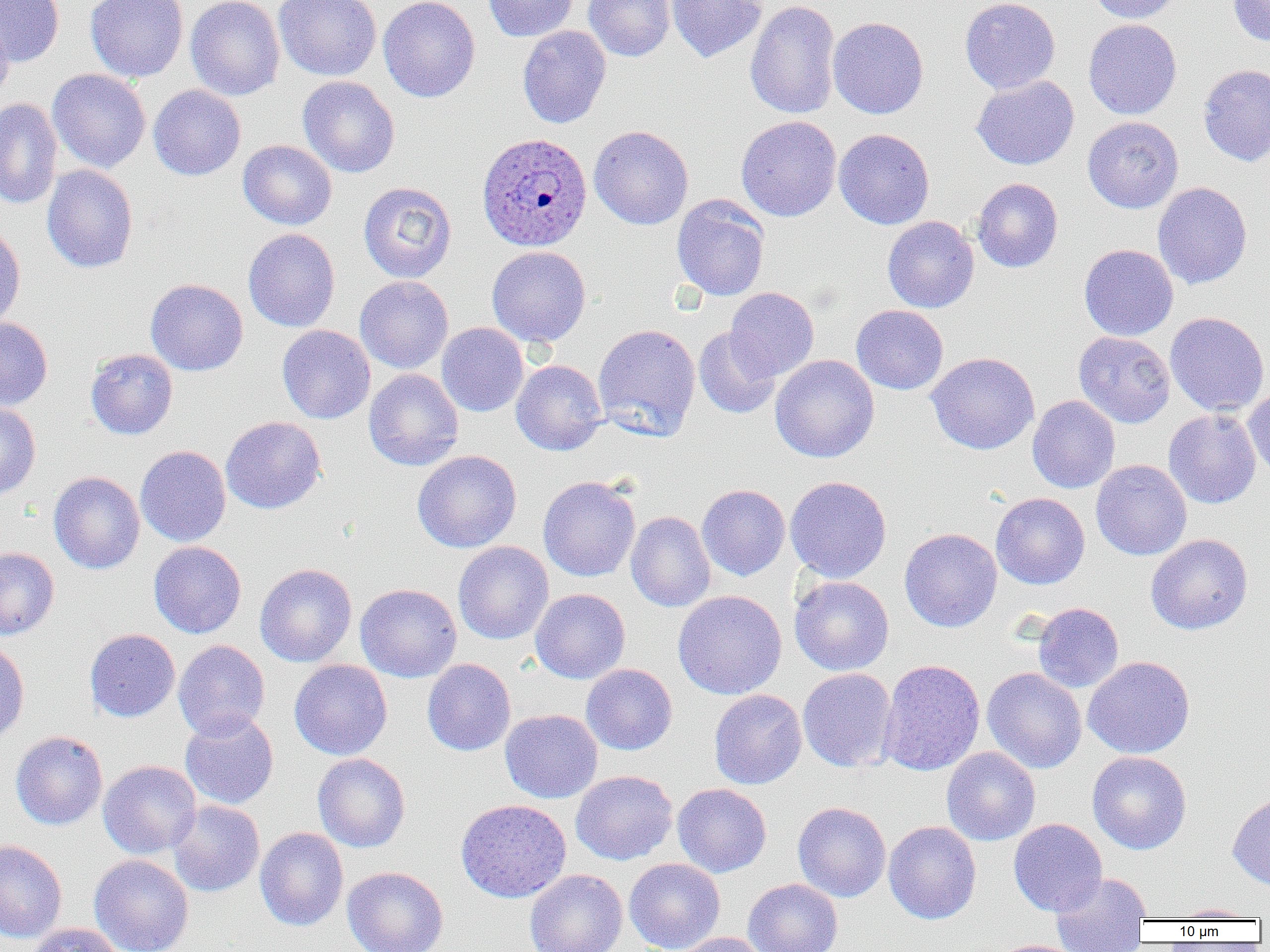

slide_level_diagnosis: Plasmodium ovale
image_size: 1270×952 pixels
plasmodium_ovale_infected_red_blood_cell_locations: 'approximate bounding boxes as (x1, y1, x2, y2) in pixels: (476, 132, 593, 252)'
modality: optical microscopy
preparation: thin blood smear
magnification: 1000x
uninfected_red_blood_cell_locations: 'approximate bounding boxes as (x1, y1, x2, y2) in pixels: (0, 0, 65, 67), (85, 0, 188, 82), (185, 0, 285, 100), (273, 0, 382, 81), (378, 0, 480, 102), (483, 0, 579, 42), (583, 0, 675, 62), (666, 0, 767, 62), (744, 0, 841, 119), (960, 0, 1060, 94), (1086, 0, 1186, 23), (1228, 1, 1270, 46), (0, 12, 14, 102), (828, 17, 929, 119), (1083, 19, 1182, 120), (517, 25, 611, 128), (1198, 63, 1270, 166), (47, 68, 151, 172), (971, 75, 1079, 170), (297, 76, 400, 178), (148, 85, 246, 180), (0, 98, 63, 209), (736, 116, 842, 222), (1083, 116, 1184, 213), (589, 125, 694, 230), (834, 128, 935, 229), (238, 140, 337, 230), (41, 164, 138, 273), (971, 178, 1063, 273), (358, 181, 457, 282), (1152, 182, 1253, 289), (671, 195, 770, 301), (882, 216, 979, 313), (0, 222, 25, 331), (243, 228, 340, 332), (1079, 244, 1178, 341), (487, 246, 591, 347), (355, 276, 453, 374), (145, 278, 248, 376), (725, 287, 819, 382), (851, 305, 948, 395), (1165, 312, 1269, 416), (0, 317, 53, 411), (436, 322, 528, 417), (593, 323, 701, 441), (277, 325, 375, 424), (693, 327, 781, 419), (1074, 331, 1176, 428), (85, 348, 178, 440), (925, 351, 1040, 455), (770, 354, 879, 463), (511, 359, 607, 455), (364, 368, 464, 471), (1243, 386, 1270, 480), (1027, 395, 1120, 493), (0, 402, 41, 502), (1163, 409, 1262, 509), (221, 416, 326, 514), (135, 445, 231, 546), (412, 450, 522, 553), (1091, 459, 1192, 560), (49, 471, 145, 574), (538, 475, 641, 582), (785, 476, 892, 583), (697, 484, 790, 581), (991, 493, 1090, 590), (626, 511, 715, 612), (899, 528, 1002, 632), (1145, 534, 1253, 635), (149, 541, 246, 638), (453, 541, 553, 645), (0, 547, 59, 640), (255, 563, 357, 667), (789, 575, 894, 675), (355, 583, 462, 682), (530, 588, 630, 683), (672, 590, 787, 700), (1033, 602, 1124, 692), (84, 629, 180, 722), (0, 638, 30, 744), (173, 640, 270, 741), (1083, 656, 1195, 759), (422, 658, 516, 755), (289, 659, 392, 760), (878, 659, 985, 776), (581, 663, 677, 755), (981, 667, 1087, 774), (798, 668, 897, 772), (709, 689, 807, 789), (500, 709, 603, 803), (180, 711, 279, 810), (10, 731, 108, 830), (941, 747, 1040, 846), (1087, 751, 1192, 854), (312, 753, 410, 853), (98, 760, 201, 858), (570, 770, 677, 865), (672, 783, 771, 877), (1227, 790, 1270, 890), (455, 798, 572, 903), (168, 800, 265, 897), (793, 801, 891, 902), (1008, 818, 1107, 916), (883, 821, 981, 924), (255, 827, 348, 931), (0, 839, 67, 942), (89, 854, 194, 952), (624, 858, 725, 952), (342, 866, 449, 952), (524, 869, 628, 952), (1050, 871, 1152, 951), (743, 878, 842, 952), (1170, 903, 1260, 921), (26, 922, 124, 952), (675, 932, 769, 952), (991, 939, 1089, 952)'
field_of_view: one of a larger specimen